Assess this cell for malaria.
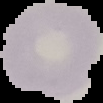

Uninfected.

Image is 103×103 pixels. From a thin blood film. Segmented cell region on a black background.